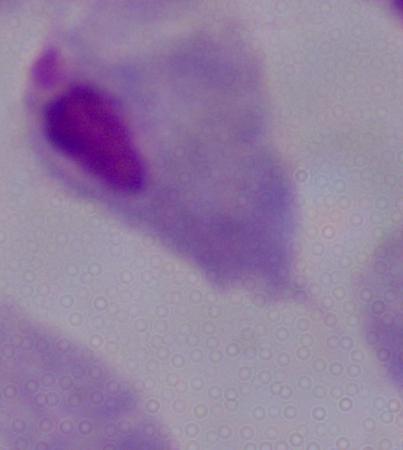
identification = trichomonad
modality = photomicrograph
magnification = 1000x